Comment on the morphology of the erythrocytes.
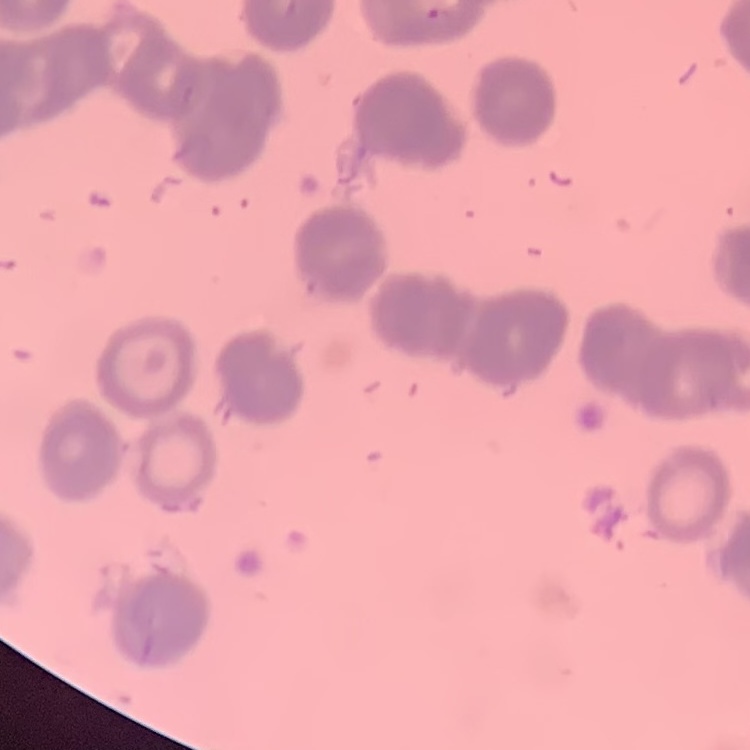
Rouleaux formation.

image_type: square crop of a larger photomicrograph
preparation: thin blood film
stain: Field's or Giemsa